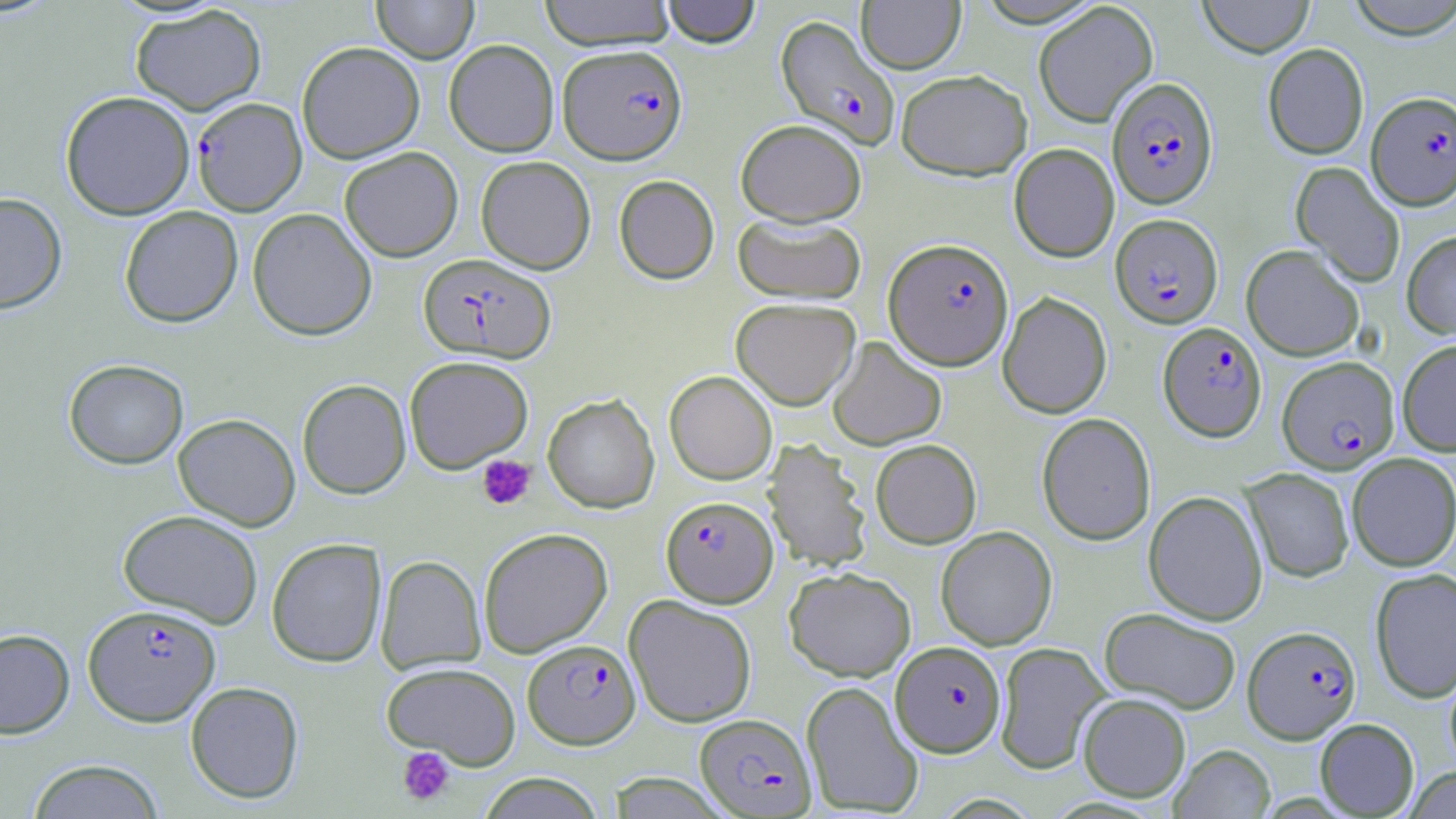
Summary:
  - Coordinate format: approximate bounding boxes as named x1/y1/x2/y2 corners in pixels
  - Uninfected red blood cell locations: (x1=371, y1=0, x2=479, y2=63), (x1=538, y1=0, x2=676, y2=50), (x1=660, y1=0, x2=761, y2=47), (x1=1198, y1=0, x2=1314, y2=57), (x1=1343, y1=0, x2=1456, y2=39), (x1=856, y1=1, x2=965, y2=74), (x1=1033, y1=2, x2=1158, y2=127), (x1=130, y1=4, x2=267, y2=115), (x1=444, y1=39, x2=559, y2=157), (x1=297, y1=41, x2=424, y2=163), (x1=1262, y1=43, x2=1368, y2=160), (x1=896, y1=69, x2=1032, y2=180), (x1=60, y1=90, x2=195, y2=220), (x1=735, y1=119, x2=866, y2=226), (x1=1009, y1=143, x2=1119, y2=262), (x1=339, y1=146, x2=463, y2=262), (x1=475, y1=155, x2=595, y2=273), (x1=1291, y1=161, x2=1405, y2=288), (x1=614, y1=175, x2=719, y2=284), (x1=0, y1=192, x2=67, y2=315), (x1=119, y1=206, x2=243, y2=327), (x1=247, y1=208, x2=377, y2=340), (x1=733, y1=213, x2=866, y2=304), (x1=1401, y1=231, x2=1456, y2=339), (x1=1241, y1=244, x2=1364, y2=361), (x1=997, y1=291, x2=1112, y2=419), (x1=730, y1=298, x2=860, y2=410), (x1=827, y1=337, x2=947, y2=450), (x1=1397, y1=339, x2=1456, y2=456), (x1=404, y1=355, x2=533, y2=473), (x1=64, y1=359, x2=188, y2=469), (x1=664, y1=371, x2=777, y2=485), (x1=298, y1=372, x2=533, y2=487), (x1=297, y1=379, x2=411, y2=498), (x1=542, y1=394, x2=659, y2=513), (x1=1036, y1=412, x2=1156, y2=545), (x1=173, y1=413, x2=301, y2=531), (x1=763, y1=439, x2=872, y2=572), (x1=870, y1=439, x2=982, y2=548), (x1=1347, y1=453, x2=1456, y2=571), (x1=1241, y1=467, x2=1354, y2=582), (x1=1144, y1=490, x2=1268, y2=625), (x1=117, y1=509, x2=264, y2=629), (x1=935, y1=526, x2=1057, y2=650), (x1=478, y1=527, x2=612, y2=657), (x1=266, y1=537, x2=387, y2=667), (x1=375, y1=555, x2=486, y2=674), (x1=784, y1=566, x2=916, y2=681), (x1=1370, y1=568, x2=1456, y2=703), (x1=624, y1=594, x2=757, y2=727), (x1=1099, y1=607, x2=1242, y2=714), (x1=0, y1=628, x2=75, y2=738), (x1=994, y1=641, x2=1110, y2=775), (x1=381, y1=661, x2=521, y2=767), (x1=1444, y1=664, x2=1456, y2=776), (x1=185, y1=681, x2=304, y2=804), (x1=801, y1=681, x2=924, y2=816), (x1=1078, y1=693, x2=1191, y2=801), (x1=1315, y1=718, x2=1419, y2=817), (x1=1170, y1=743, x2=1275, y2=818), (x1=26, y1=758, x2=165, y2=818), (x1=1402, y1=766, x2=1456, y2=819), (x1=477, y1=772, x2=607, y2=818), (x1=607, y1=773, x2=731, y2=817)
  - Plasmodium falciparum-infected red blood cell locations: (x1=776, y1=15, x2=899, y2=148), (x1=558, y1=43, x2=687, y2=165), (x1=1107, y1=76, x2=1218, y2=208), (x1=1366, y1=91, x2=1456, y2=210), (x1=192, y1=97, x2=307, y2=216), (x1=1110, y1=213, x2=1223, y2=328), (x1=884, y1=238, x2=1014, y2=370), (x1=418, y1=253, x2=556, y2=363), (x1=1158, y1=322, x2=1266, y2=441), (x1=1278, y1=356, x2=1399, y2=473), (x1=661, y1=496, x2=778, y2=607), (x1=83, y1=604, x2=221, y2=726), (x1=1243, y1=625, x2=1361, y2=743), (x1=522, y1=639, x2=640, y2=749), (x1=890, y1=640, x2=1006, y2=756), (x1=695, y1=713, x2=816, y2=817)
  - Platelet locations: (x1=477, y1=455, x2=536, y2=510), (x1=397, y1=747, x2=456, y2=806)
  - Slide-level diagnosis: Plasmodium falciparum
  - Preparation: thin blood smear
  - Image size: 1456×819 pixels
  - Stain: May-Grünwald-Giemsa
  - Modality: optical microscopy
  - Magnification: 1000x
  - Field of view: single